Point out each Plasmodium parasite.
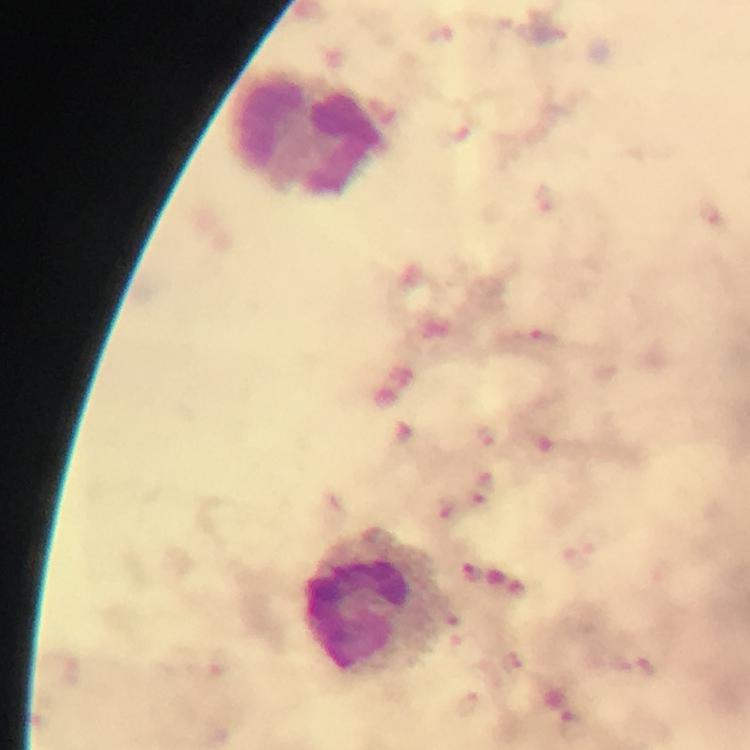

Approximate object centers, in pixels from the top-left corner.
Plasmodium parasites: (x=546, y=198), (x=712, y=213), (x=538, y=339), (x=491, y=434), (x=486, y=481), (x=477, y=499), (x=446, y=507), (x=469, y=705).

preparation = thick smear
stain = Giemsa
image size = 750×750 pixels
capture = smartphone mounted on the microscope
leukocyte locations = approximate object centers, in pixels from the top-left corner: (x=310, y=134), (x=379, y=603)
immersion oil = applied
magnification = 100x
cropped from = a single field of view
context = from a diagnostic examination for malaria